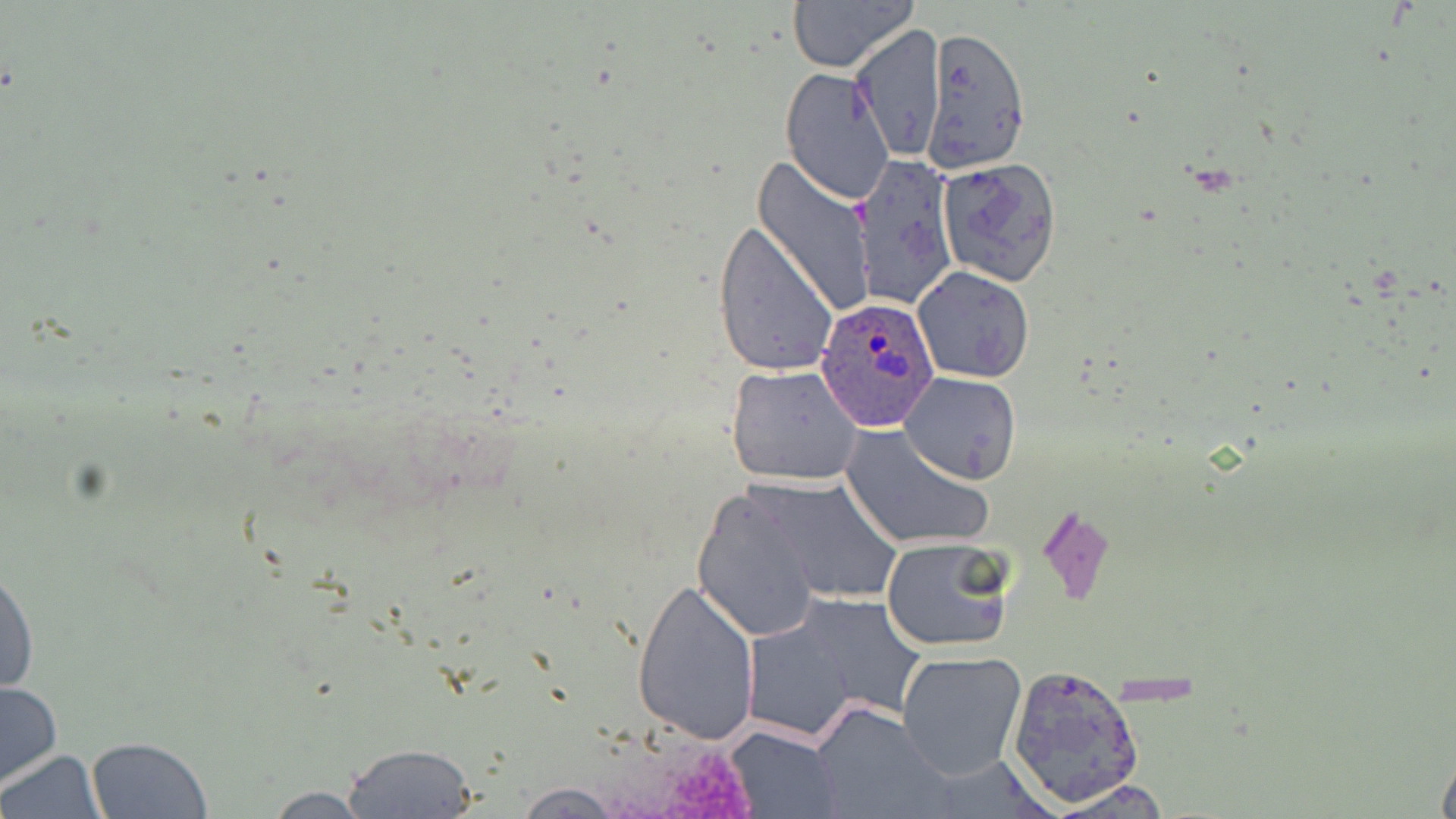

{
  "slide_level_diagnosis": "Plasmodium ovale",
  "image_size": "1456×819 pixels",
  "modality": "light microscopy",
  "field_of_view": "one of a larger specimen",
  "plasmodium_ovale_infected_red_blood_cell_locations": "approximate bounding boxes as (x1, y1, x2, y2) in pixels: (815, 292, 941, 433)",
  "preparation": "thin blood smear",
  "magnification": "1000x",
  "stain": "May-Grünwald-Giemsa",
  "uninfected_red_blood_cell_locations": "approximate bounding boxes as (x1, y1, x2, y2) in pixels: (787, 0, 919, 72), (849, 24, 946, 162), (921, 26, 1032, 175), (781, 68, 897, 207), (851, 151, 958, 311), (751, 156, 874, 317), (936, 159, 1062, 286), (713, 218, 838, 379), (913, 266, 1035, 384), (726, 363, 862, 485), (898, 371, 1023, 485), (840, 424, 995, 552), (754, 475, 905, 604), (692, 487, 824, 642), (880, 535, 1015, 653), (0, 560, 39, 699), (632, 574, 761, 748), (748, 593, 926, 739), (897, 649, 1027, 779), (1006, 662, 1145, 809), (0, 679, 62, 789), (811, 702, 947, 819), (724, 725, 842, 819), (85, 736, 214, 819), (342, 742, 479, 817), (1435, 742, 1456, 819), (1, 749, 104, 818), (511, 782, 626, 817), (255, 786, 380, 817)"
}